State which parasite is depicted.
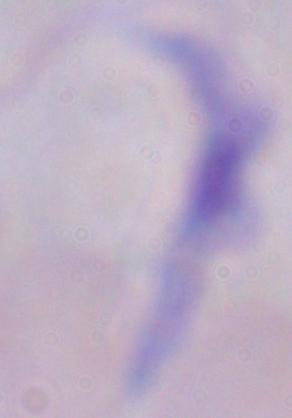
A trypanosome.

Photomicrograph. 1000x magnification.